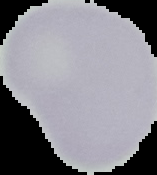
Summary:
  - Image size: 157×175 pixels
  - Result: no malaria parasites detected
  - Image type: cell region segmented out of the field of view; surrounding area masked to black
  - Preparation: thin blood smear